Give the position of every malaria parasite and every leukocyte.
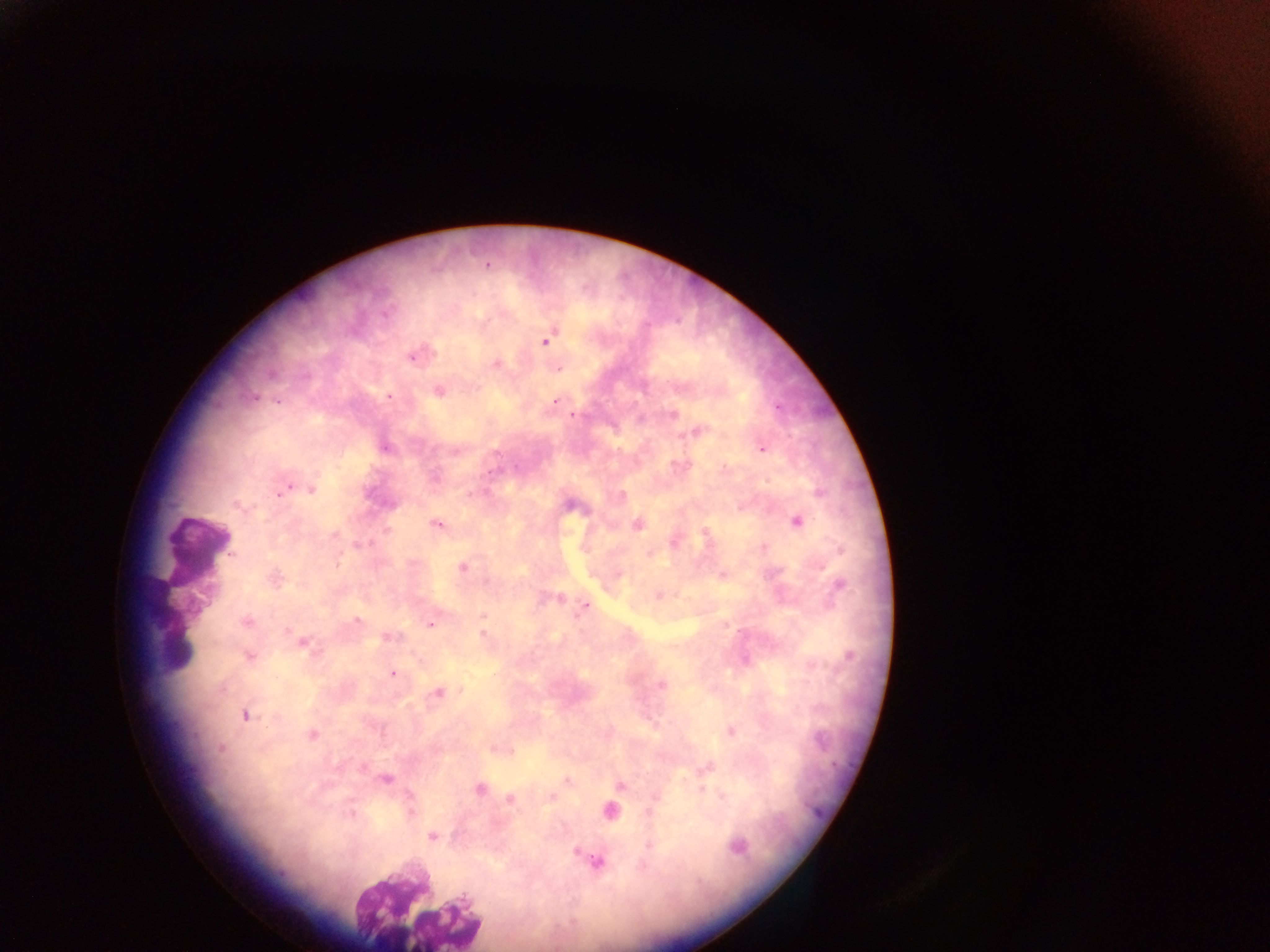

Approximate centers as [x, y] in pixels.
Malaria parasites: [487, 265], [546, 339], [415, 354], [495, 364], [558, 368], [438, 391], [388, 396], [555, 402], [573, 414], [672, 414], [696, 431], [384, 446], [762, 447], [284, 487], [311, 488], [569, 503], [796, 520], [437, 524], [637, 524], [705, 533], [360, 545], [463, 567], [723, 574], [275, 578], [659, 595], [556, 598], [583, 607], [483, 616], [246, 621], [356, 621], [430, 623], [483, 627], [483, 635], [389, 636], [303, 643], [248, 656], [393, 673], [661, 684], [438, 693], [245, 715], [730, 731], [312, 735], [499, 748], [706, 768], [385, 779], [567, 780], [620, 785], [478, 788], [550, 798], [510, 799], [609, 810], [431, 836], [736, 846], [595, 860].
Leukocytes: [196, 548], [150, 603], [173, 658].

image size = 1270×952 pixels
field of view = single
country = Ghana
capture = mobile-phone photograph through a microscope
preparation = thick blood film